Classify this cell by malaria status.
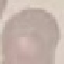

Uninfected.

Summary:
  - Image type: automatically extracted cell patch, resized to 64 × 64 pixels
  - Preparation: thin blood film
  - Stain: Giemsa
  - Capture: smartphone through the microscope eyepiece